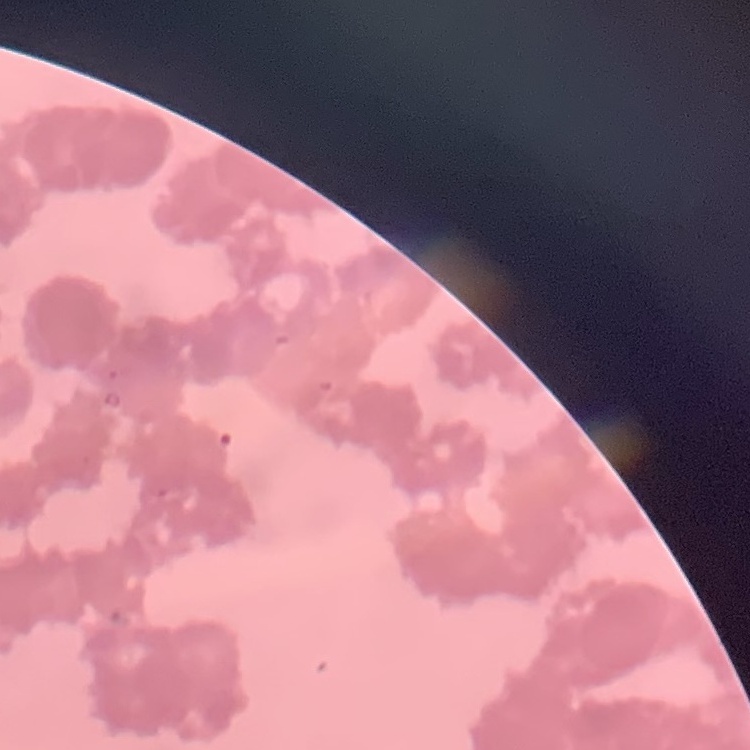
red blood cell morphology = rouleaux formation
image type = square crop of a larger photomicrograph
preparation = thin blood smear
stain = Field's or Giemsa